Classify this cell by malaria status.
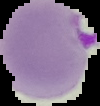
Parasitized.

Summary:
  - Preparation: thin blood film
  - Image type: cell region segmented out of the field of view; surrounding area masked to black
  - Image size: 100×106 pixels